Assess this cell for malaria.
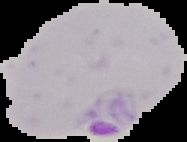

Parasitized.

Summary:
  - Image type: cell region segmented out of the field of view; surrounding area masked to black
  - Image size: 187×142 pixels
  - Preparation: thin blood smear